Name the blood parasite species.
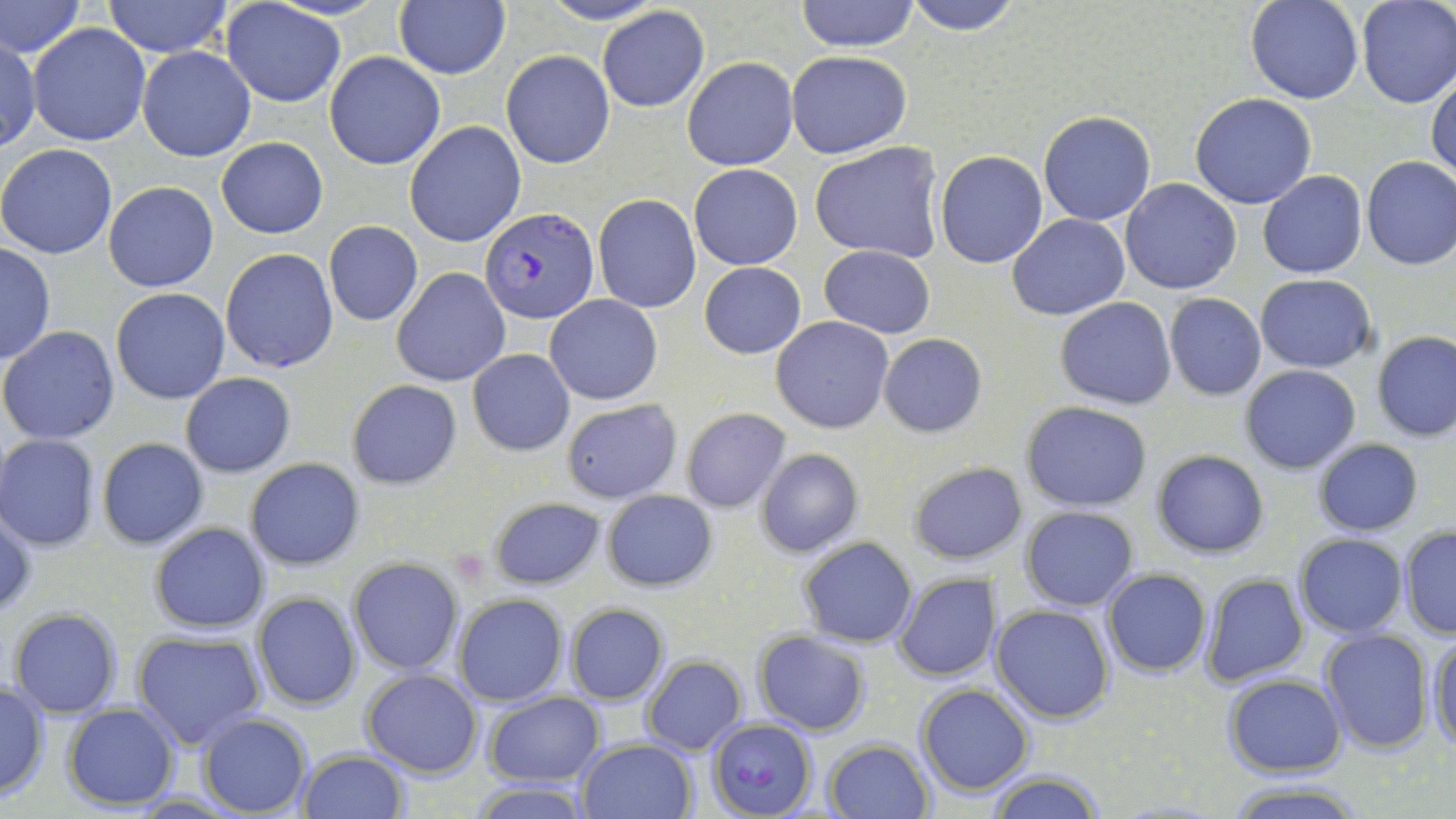

Plasmodium falciparum.

Summary:
  - Coordinate format: approximate bounding boxes as [x1, y1, x2, y2] in pixels
  - Platelet locations: [449, 547, 489, 587]
  - Uninfected red blood cell locations: [1, 0, 84, 61], [101, 0, 234, 57], [536, 0, 665, 25], [794, 0, 920, 52], [902, 0, 1024, 34], [1245, 0, 1363, 104], [1355, 0, 1455, 109], [220, 2, 346, 107], [394, 2, 510, 80], [597, 6, 709, 113], [27, 22, 150, 147], [1, 37, 40, 152], [137, 46, 256, 162], [502, 50, 615, 170], [785, 51, 911, 159], [324, 52, 446, 170], [682, 56, 797, 171], [1427, 72, 1456, 184], [1190, 93, 1317, 210], [1038, 110, 1156, 226], [404, 121, 526, 248], [215, 137, 328, 239], [810, 141, 947, 263], [0, 143, 119, 259], [935, 150, 1048, 268], [1361, 157, 1456, 270], [689, 162, 803, 270], [1258, 170, 1368, 278], [1119, 178, 1243, 294], [102, 181, 219, 292], [593, 193, 701, 313], [1007, 214, 1130, 320], [323, 220, 424, 326], [0, 243, 55, 366], [819, 245, 936, 338], [221, 247, 338, 374], [699, 261, 806, 359], [390, 267, 509, 387], [1255, 274, 1378, 373], [111, 288, 230, 404], [544, 294, 663, 406], [1164, 294, 1267, 400], [1055, 297, 1178, 409], [771, 316, 894, 434], [1, 325, 120, 446], [1372, 331, 1456, 441], [879, 332, 985, 436], [467, 349, 574, 456], [1240, 364, 1362, 474], [180, 372, 296, 477], [346, 379, 463, 490], [561, 398, 682, 503], [1020, 401, 1153, 512], [680, 407, 791, 513], [1, 434, 101, 551], [96, 437, 209, 551], [1312, 437, 1424, 535], [755, 448, 863, 557], [1152, 450, 1269, 557], [245, 457, 365, 570], [907, 461, 1026, 565], [600, 489, 718, 591], [488, 494, 606, 592], [1019, 505, 1139, 610], [0, 509, 37, 621], [148, 522, 271, 634], [1400, 527, 1456, 640], [1296, 533, 1409, 638], [798, 536, 918, 646], [347, 557, 463, 675], [1101, 569, 1211, 677], [1200, 572, 1309, 685], [895, 573, 996, 680], [252, 592, 360, 710], [453, 593, 568, 706], [990, 603, 1114, 724], [564, 604, 669, 704], [9, 608, 121, 716], [1318, 628, 1433, 754], [1426, 629, 1455, 751], [753, 631, 870, 735], [133, 632, 268, 751], [642, 655, 747, 754], [360, 668, 482, 777], [1224, 674, 1345, 776], [0, 679, 50, 801], [917, 683, 1034, 797], [483, 691, 606, 786], [62, 703, 180, 809], [196, 713, 313, 817], [577, 739, 696, 819], [825, 739, 934, 819], [296, 748, 409, 818], [985, 767, 1109, 819], [467, 781, 595, 818], [1224, 783, 1369, 818]
  - Plasmodium falciparum-infected red blood cell locations: [480, 207, 599, 324], [707, 716, 816, 816]
  - Stain: May-Grünwald-Giemsa
  - Preparation: thin blood smear
  - Image size: 1456×819 pixels
  - Field of view: one of a larger specimen
  - Magnification: 1000x
  - Modality: light microscopy